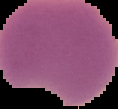
From a thin blood film. Cell region segmented out of the field of view; the surrounding area is masked to black. Malaria status: parasitized. Image is 118×109 pixels.